Locate every malaria parasite.
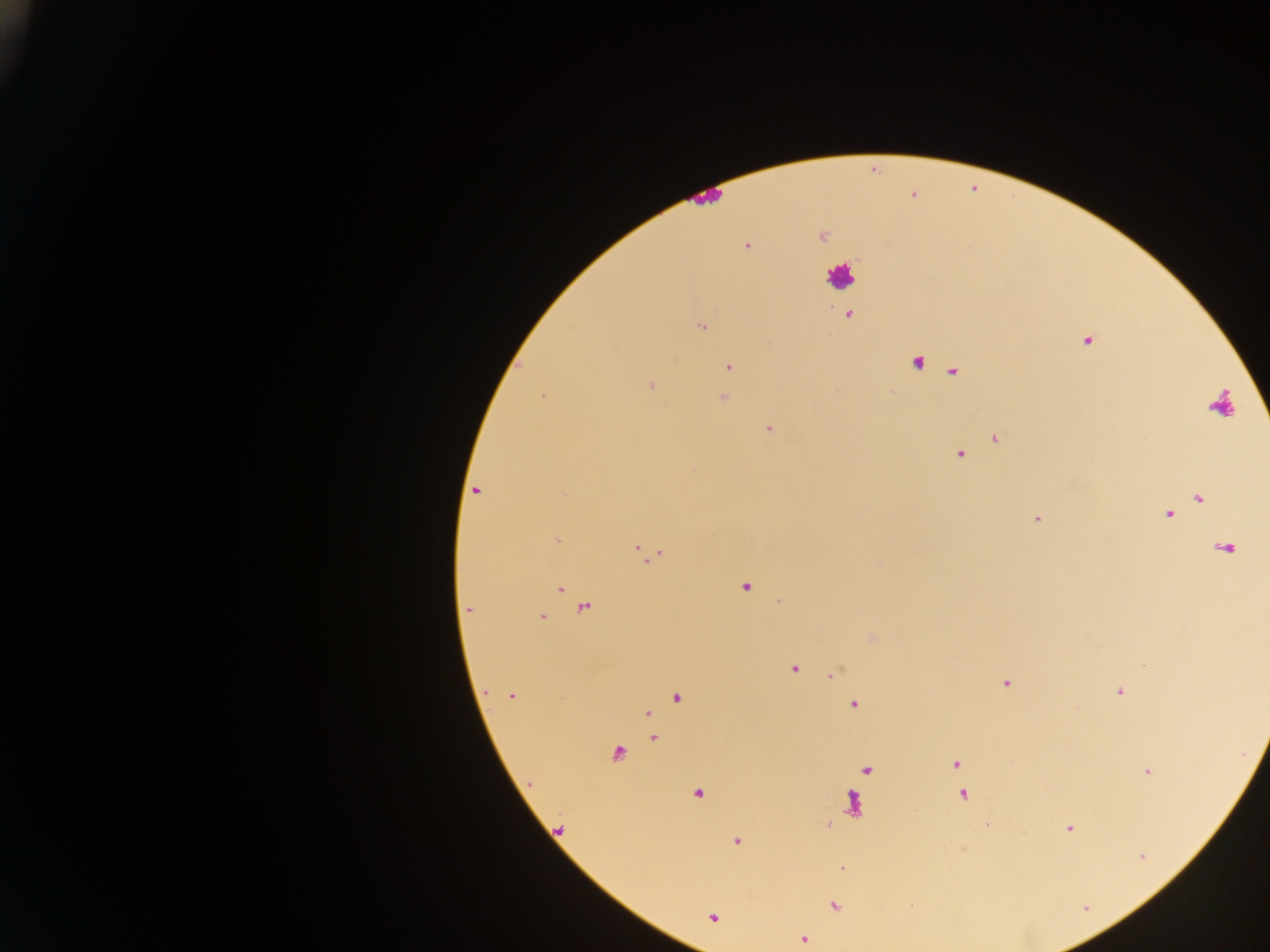
Approximate centers as {x, y} in pixels.
Malaria parasites: {821, 234}, {746, 246}, {849, 315}, {701, 326}, {1087, 339}, {916, 361}, {727, 366}, {952, 370}, {651, 384}, {891, 391}, {542, 395}, {722, 398}, {768, 429}, {996, 438}, {959, 454}, {476, 490}, {1199, 496}, {1168, 513}, {1037, 518}, {557, 540}, {1224, 547}, {646, 553}, {745, 586}, {560, 587}, {781, 601}, {584, 607}, {469, 608}, {541, 617}, {871, 637}, {793, 668}, {832, 674}, {1006, 684}, {1119, 691}, {511, 696}, {678, 697}, {853, 703}, {646, 712}, {653, 737}, {616, 752}, {954, 764}, {867, 770}, {1147, 771}, {697, 792}, {963, 795}, {987, 824}, {1068, 828}, {558, 829}, {735, 841}, {842, 867}, {835, 905}, {712, 917}, {803, 939}.
Each of these objects is labeled both malaria parasite and leukocyte by the source: {1220, 403}, {852, 805}.

Summary:
  - Leukocyte locations: {706, 196}, {839, 276}
  - Preparation: thick blood film
  - Country: Ghana
  - Capture: mobile-phone photograph through a microscope
  - Field of view: single
  - Image size: 1270×952 pixels